Name the cell type shown.
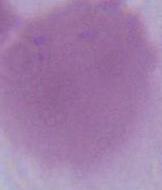

An erythrocyte.

1000x magnification. Photomicrograph.